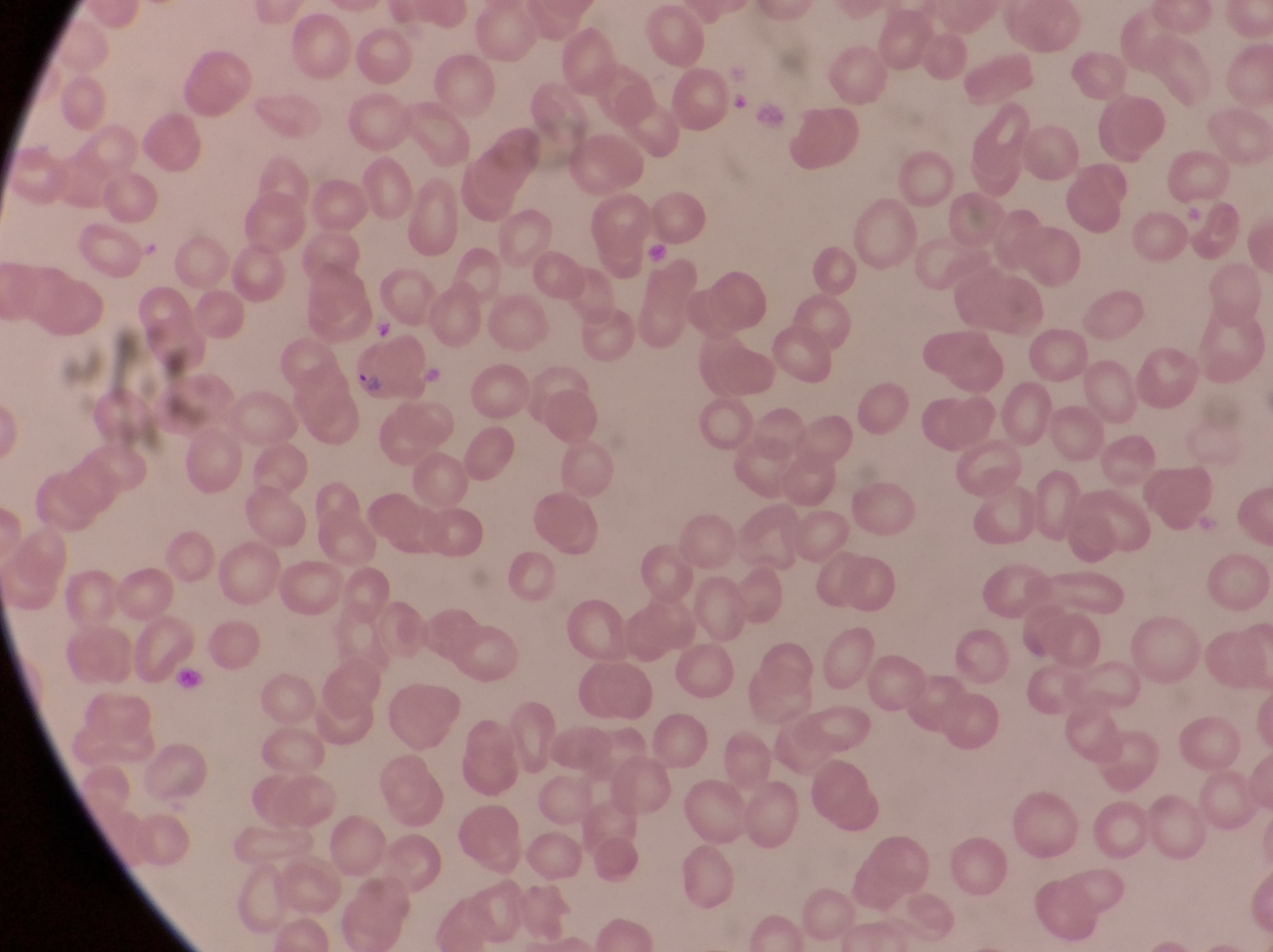
parasitised red blood cell locations = approximate bounding boxes as left top right bottom in pixels: 350 345 438 410
image size = 1273×952 pixels
preparation = thin blood film
country = Uganda
field of view = single
artifact (platelet-like body, stain precipitate, or debris) locations = approximate bounding boxes as left top right bottom in pixels: 641 235 674 268; 174 665 210 702
capture = smartphone photograph through the eyepiece of an Olympus CX-23 microscope
magnification = 1000x